State which parasite is depicted.
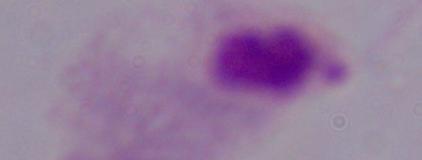
This is a trichomonad.

Photomicrograph. 1000x magnification.